Locate every malaria parasite.
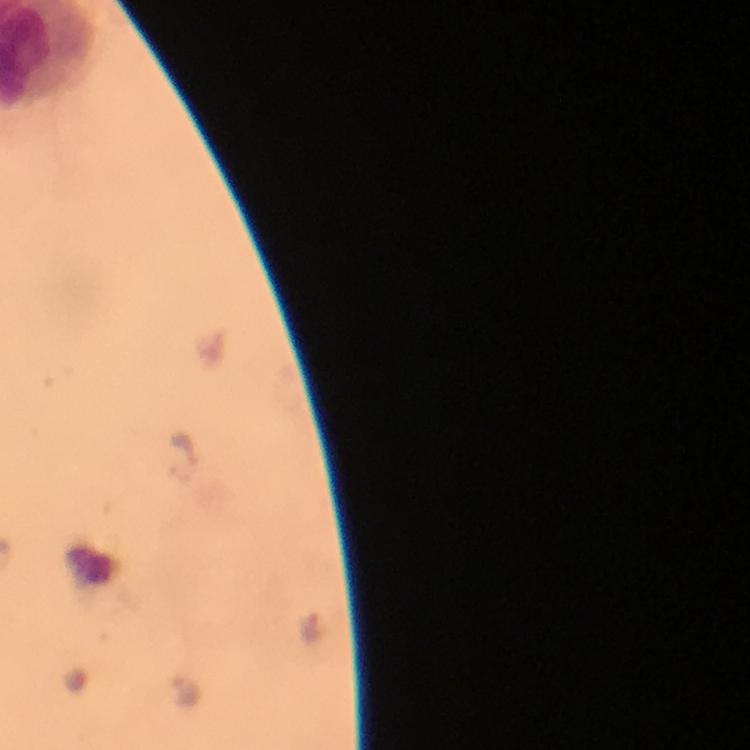
Approximate centers as {x, y} in pixels.
Malaria parasites: {179, 459}, {305, 631}, {183, 690}.

Summary:
  - Preparation: thick blood film
  - Immersion oil: used
  - Stain: Giemsa
  - Cropped from: one field of view
  - Context: from a diagnostic examination for malaria
  - Image size: 750×750 pixels
  - Capture: smartphone camera through the microscope
  - Magnification: 100x